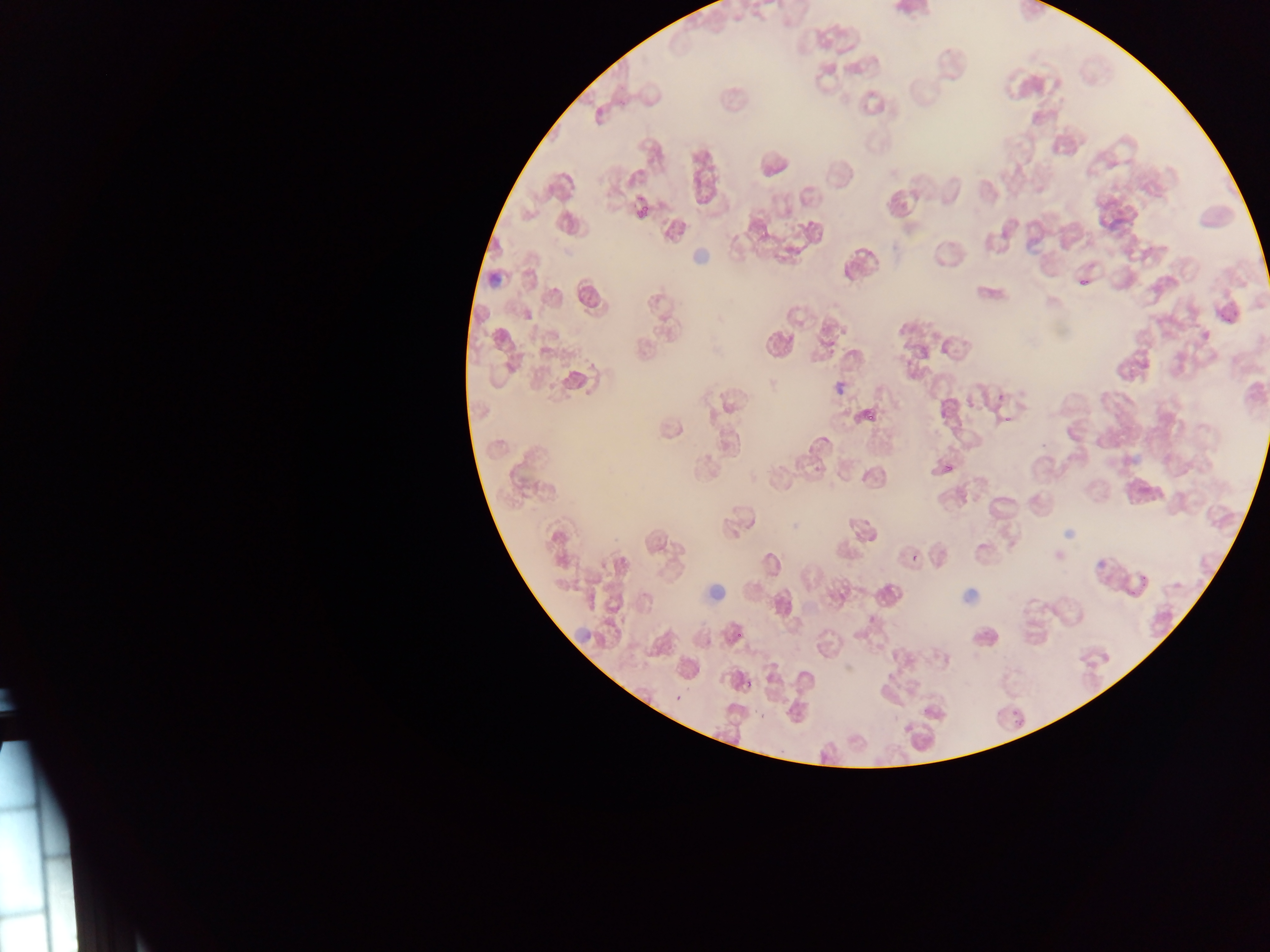
{
  "country": "Ghana",
  "capture": "mobile-phone photograph through a microscope",
  "image_size": "1270×952 pixels",
  "leukocyte_locations": "approximate bounding boxes as left top right bottom in pixels: 689 246 715 269; 485 270 505 287; 708 578 729 607; 959 587 982 606; 569 621 595 646",
  "preparation": "thin blood film",
  "malaria_parasite_locations": "approximate bounding boxes as left top right bottom in pixels: 1080 280 1088 288; 1232 310 1240 317; 910 553 918 561; 1130 578 1150 599; 745 679 753 689; 675 694 682 702; 758 710 769 719; 1015 719 1025 726 | approximate x y pixel centers of objects too small to bound: 1222 315; 1228 320; 870 417; 1008 419; 740 635",
  "field_of_view": "single"
}